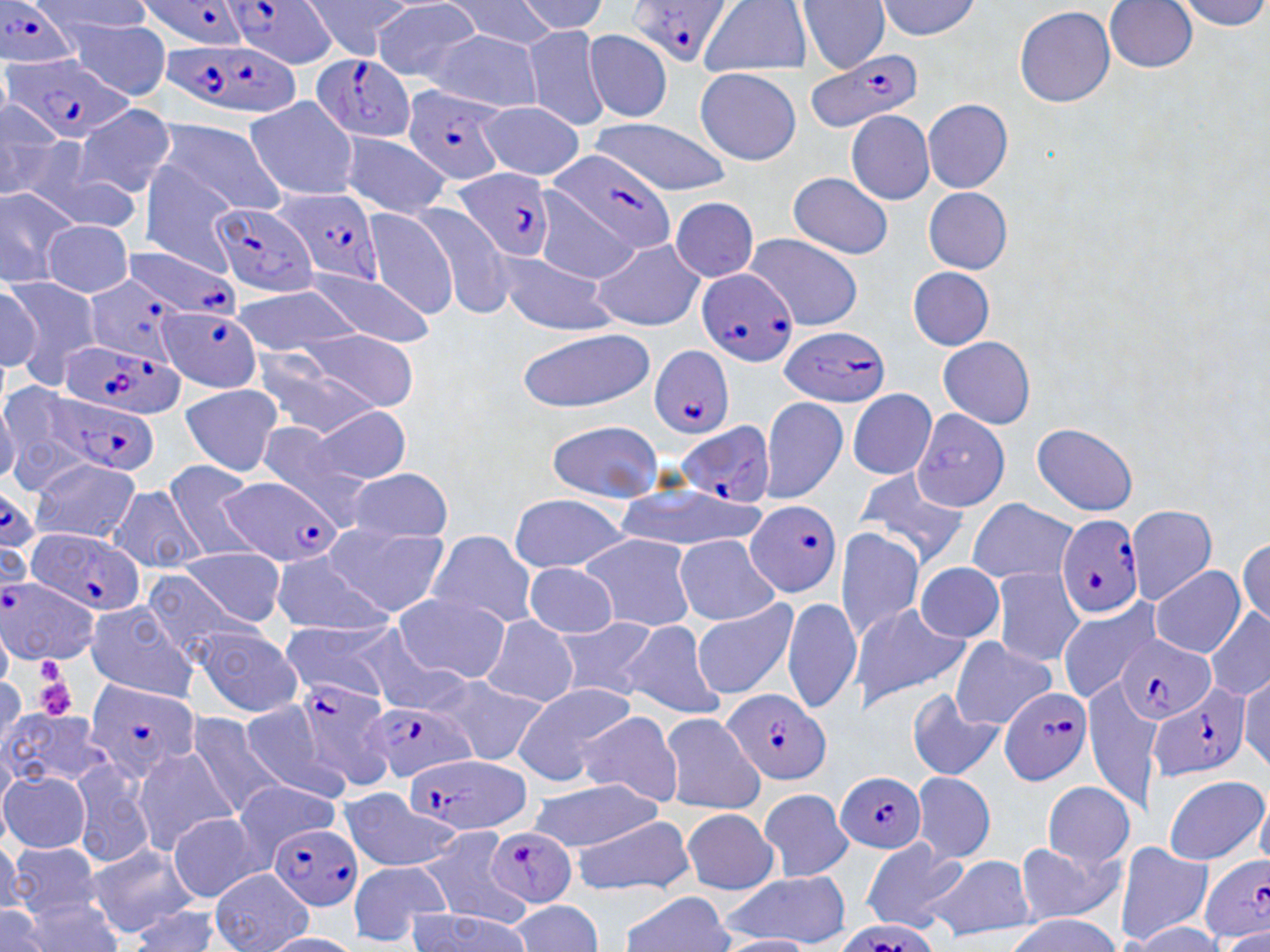

slide-level diagnosis = Plasmodium falciparum
stain = May-Grünwald-Giemsa
magnification = 1000x
uninfected red blood cell locations = approximate bounding boxes as named x1/y1/x2/y2 corners in pixels: (x1=302, y1=0, x2=410, y2=62), (x1=447, y1=0, x2=557, y2=49), (x1=701, y1=0, x2=816, y2=78), (x1=793, y1=0, x2=886, y2=68), (x1=879, y1=0, x2=983, y2=46), (x1=1100, y1=0, x2=1197, y2=73), (x1=371, y1=1, x2=480, y2=82), (x1=1012, y1=5, x2=1114, y2=107), (x1=53, y1=15, x2=170, y2=102), (x1=525, y1=26, x2=609, y2=128), (x1=587, y1=26, x2=670, y2=123), (x1=408, y1=32, x2=545, y2=111), (x1=696, y1=66, x2=799, y2=163), (x1=246, y1=97, x2=359, y2=199), (x1=923, y1=97, x2=1010, y2=192), (x1=478, y1=103, x2=586, y2=182), (x1=69, y1=104, x2=178, y2=198), (x1=846, y1=107, x2=937, y2=208), (x1=158, y1=117, x2=292, y2=216), (x1=592, y1=120, x2=729, y2=192), (x1=340, y1=126, x2=445, y2=220), (x1=1, y1=132, x2=141, y2=231), (x1=138, y1=155, x2=238, y2=281), (x1=787, y1=171, x2=895, y2=259), (x1=921, y1=186, x2=1011, y2=274), (x1=1, y1=189, x2=72, y2=287), (x1=672, y1=196, x2=756, y2=282), (x1=418, y1=202, x2=513, y2=322), (x1=368, y1=208, x2=456, y2=321), (x1=44, y1=223, x2=130, y2=297), (x1=745, y1=232, x2=864, y2=317), (x1=590, y1=240, x2=707, y2=332), (x1=495, y1=248, x2=617, y2=336), (x1=304, y1=264, x2=433, y2=346), (x1=901, y1=265, x2=999, y2=353), (x1=3, y1=275, x2=97, y2=391), (x1=231, y1=284, x2=362, y2=354), (x1=301, y1=326, x2=415, y2=410), (x1=515, y1=329, x2=659, y2=407), (x1=935, y1=336, x2=1037, y2=428), (x1=251, y1=344, x2=382, y2=440), (x1=0, y1=381, x2=83, y2=499), (x1=175, y1=384, x2=283, y2=475), (x1=847, y1=390, x2=935, y2=485), (x1=765, y1=396, x2=851, y2=505), (x1=299, y1=403, x2=412, y2=484), (x1=910, y1=412, x2=1010, y2=512), (x1=550, y1=419, x2=660, y2=497), (x1=1029, y1=420, x2=1146, y2=506), (x1=28, y1=460, x2=143, y2=543), (x1=165, y1=461, x2=262, y2=561), (x1=853, y1=465, x2=971, y2=565), (x1=345, y1=470, x2=452, y2=544), (x1=614, y1=483, x2=767, y2=546), (x1=106, y1=487, x2=211, y2=573), (x1=508, y1=495, x2=631, y2=570), (x1=968, y1=496, x2=1074, y2=582), (x1=1134, y1=503, x2=1214, y2=607), (x1=327, y1=522, x2=448, y2=616), (x1=838, y1=526, x2=923, y2=644), (x1=420, y1=529, x2=535, y2=625), (x1=578, y1=534, x2=694, y2=632), (x1=677, y1=535, x2=779, y2=622), (x1=177, y1=547, x2=289, y2=625), (x1=267, y1=553, x2=396, y2=633), (x1=914, y1=559, x2=1007, y2=643), (x1=522, y1=564, x2=618, y2=642), (x1=1150, y1=564, x2=1248, y2=658), (x1=994, y1=566, x2=1085, y2=668), (x1=395, y1=594, x2=507, y2=683), (x1=1061, y1=597, x2=1140, y2=702), (x1=83, y1=598, x2=202, y2=703), (x1=696, y1=598, x2=797, y2=700), (x1=784, y1=599, x2=861, y2=715), (x1=855, y1=603, x2=969, y2=711), (x1=476, y1=617, x2=577, y2=708), (x1=555, y1=617, x2=654, y2=701), (x1=279, y1=619, x2=392, y2=701), (x1=348, y1=620, x2=471, y2=714), (x1=615, y1=620, x2=725, y2=719), (x1=187, y1=627, x2=302, y2=714), (x1=949, y1=634, x2=1059, y2=725), (x1=421, y1=674, x2=546, y2=765), (x1=512, y1=683, x2=634, y2=783), (x1=908, y1=690, x2=1003, y2=782), (x1=239, y1=697, x2=315, y2=794), (x1=189, y1=703, x2=287, y2=818), (x1=563, y1=711, x2=680, y2=806), (x1=0, y1=713, x2=116, y2=789), (x1=662, y1=713, x2=765, y2=813), (x1=134, y1=744, x2=237, y2=859), (x1=72, y1=758, x2=152, y2=865), (x1=913, y1=771, x2=995, y2=864), (x1=1165, y1=772, x2=1269, y2=860), (x1=2, y1=774, x2=89, y2=853), (x1=235, y1=779, x2=338, y2=848), (x1=532, y1=781, x2=665, y2=850), (x1=1042, y1=783, x2=1136, y2=867), (x1=338, y1=787, x2=427, y2=870), (x1=758, y1=789, x2=850, y2=881), (x1=679, y1=807, x2=779, y2=895), (x1=573, y1=816, x2=696, y2=895), (x1=169, y1=817, x2=254, y2=904), (x1=419, y1=827, x2=519, y2=930), (x1=5, y1=838, x2=111, y2=921), (x1=860, y1=840, x2=964, y2=934), (x1=73, y1=841, x2=197, y2=937), (x1=1015, y1=842, x2=1126, y2=923), (x1=1117, y1=843, x2=1213, y2=942), (x1=917, y1=857, x2=1040, y2=941), (x1=351, y1=861, x2=453, y2=947), (x1=196, y1=872, x2=314, y2=940), (x1=720, y1=872, x2=848, y2=949), (x1=618, y1=891, x2=740, y2=951), (x1=506, y1=900, x2=603, y2=952)
preparation = thin blood film
Plasmodium falciparum-infected red blood cell locations = approximate bounding boxes as named x1/y1/x2/y2 corners in pixels: (x1=139, y1=0, x2=249, y2=56), (x1=224, y1=0, x2=336, y2=74), (x1=622, y1=0, x2=729, y2=68), (x1=2, y1=1, x2=79, y2=71), (x1=157, y1=43, x2=305, y2=118), (x1=807, y1=48, x2=923, y2=129), (x1=308, y1=52, x2=417, y2=145), (x1=1, y1=60, x2=135, y2=146), (x1=402, y1=83, x2=504, y2=189), (x1=548, y1=149, x2=676, y2=251), (x1=454, y1=167, x2=555, y2=259), (x1=268, y1=185, x2=399, y2=288), (x1=211, y1=206, x2=324, y2=295), (x1=122, y1=249, x2=242, y2=321), (x1=697, y1=269, x2=801, y2=367), (x1=88, y1=275, x2=183, y2=368), (x1=152, y1=308, x2=263, y2=392), (x1=780, y1=328, x2=890, y2=407), (x1=61, y1=342, x2=187, y2=417), (x1=645, y1=343, x2=736, y2=442), (x1=38, y1=392, x2=156, y2=477), (x1=674, y1=419, x2=775, y2=506), (x1=216, y1=475, x2=343, y2=567), (x1=747, y1=497, x2=842, y2=595), (x1=1060, y1=514, x2=1144, y2=620), (x1=23, y1=527, x2=148, y2=617), (x1=0, y1=577, x2=99, y2=662), (x1=1118, y1=632, x2=1215, y2=725), (x1=81, y1=676, x2=202, y2=783), (x1=298, y1=677, x2=398, y2=791), (x1=1149, y1=683, x2=1251, y2=789), (x1=997, y1=684, x2=1092, y2=787), (x1=722, y1=687, x2=830, y2=784), (x1=356, y1=702, x2=481, y2=785), (x1=398, y1=760, x2=540, y2=834), (x1=833, y1=769, x2=929, y2=855), (x1=486, y1=826, x2=580, y2=907), (x1=269, y1=828, x2=361, y2=911), (x1=1198, y1=855, x2=1270, y2=944), (x1=837, y1=920, x2=931, y2=950)
image size = 1270×952 pixels
platelet locations = approximate bounding boxes as named x1/y1/x2/y2 corners in pixels: (x1=35, y1=655, x2=66, y2=683), (x1=35, y1=681, x2=78, y2=716)
modality = light microscopy
field of view = single